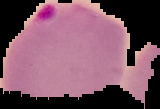

Malaria status: parasitized. Image is 160×109 pixels. From a thin blood film. Segmented cell region on a black background.